Give the extent of all Trypanosoma brucei.
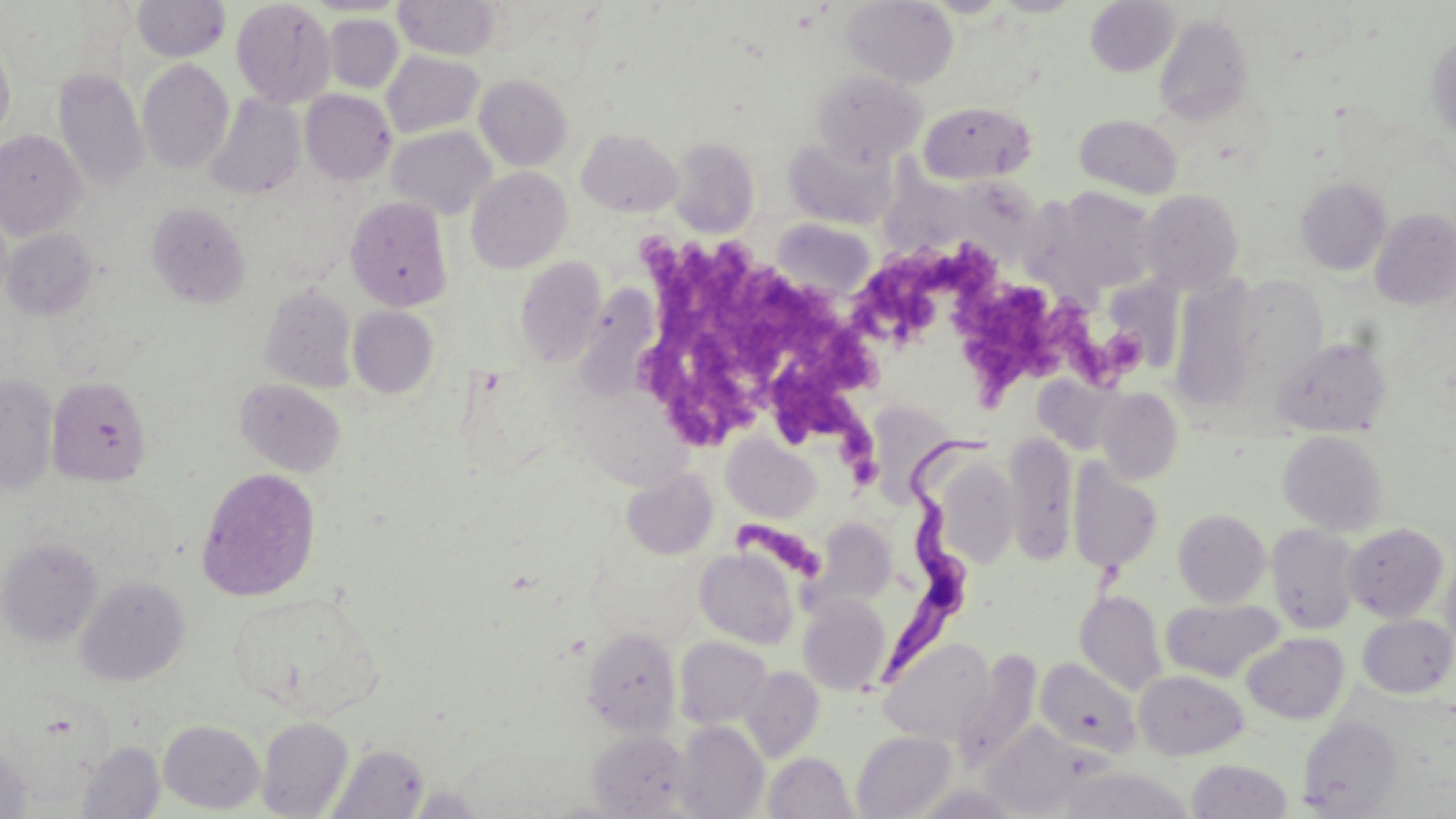
Approximate bounding boxes as [x1, y1, x2, y2] in pixels.
Trypanosoma brucei: [879, 432, 1000, 686].

Platelet locations: [631, 230, 779, 440], [865, 250, 996, 342], [772, 279, 886, 483], [960, 281, 1079, 404], [1059, 307, 1142, 388], [731, 523, 823, 577]. Uninfected red blood cell locations: [132, 0, 231, 62], [393, 0, 501, 60], [920, 0, 1015, 18], [991, 0, 1087, 16], [232, 1, 336, 108], [842, 1, 959, 88], [1085, 1, 1180, 77], [325, 14, 403, 94], [1154, 14, 1254, 125], [1426, 32, 1456, 141], [0, 40, 15, 145], [381, 51, 484, 138], [137, 59, 234, 174], [53, 69, 148, 191], [811, 69, 927, 167], [474, 75, 573, 171], [301, 89, 396, 185], [205, 94, 305, 199], [919, 101, 1037, 184], [1075, 114, 1183, 199], [387, 126, 496, 220], [577, 128, 682, 217], [0, 130, 88, 240], [669, 137, 760, 237], [784, 137, 898, 230], [882, 152, 971, 258], [466, 166, 572, 273], [963, 172, 1059, 274], [1296, 177, 1392, 276], [1049, 187, 1158, 291], [1140, 190, 1244, 294], [345, 196, 452, 311], [147, 201, 251, 309], [1370, 207, 1456, 311], [772, 218, 876, 302], [2, 228, 97, 321], [515, 256, 607, 367], [1228, 275, 1328, 385], [1103, 279, 1184, 372], [1172, 279, 1258, 412], [259, 282, 357, 393], [347, 306, 439, 398], [1272, 336, 1392, 438], [0, 373, 58, 495], [47, 376, 152, 487], [234, 379, 346, 477], [1097, 387, 1184, 484], [870, 401, 959, 505], [1278, 431, 1389, 535], [1004, 432, 1077, 564], [723, 436, 821, 523], [935, 457, 1019, 568], [1068, 460, 1162, 574], [196, 467, 321, 601], [621, 469, 717, 560], [1173, 509, 1271, 608], [810, 518, 896, 611], [1343, 523, 1449, 622], [1266, 524, 1362, 634], [1, 537, 103, 647], [694, 547, 799, 649], [1440, 553, 1456, 657], [76, 576, 190, 686], [227, 589, 383, 720], [1075, 590, 1167, 695], [797, 594, 891, 695], [1161, 598, 1284, 683], [1357, 614, 1456, 698], [582, 627, 681, 737], [1242, 632, 1349, 724], [674, 636, 772, 729], [880, 638, 995, 746], [953, 647, 1041, 770], [1036, 657, 1141, 757], [740, 666, 824, 762], [1134, 670, 1248, 760], [1298, 715, 1404, 817], [256, 717, 354, 818], [158, 720, 265, 813], [673, 721, 769, 818], [982, 727, 1088, 813], [588, 729, 691, 818], [851, 730, 957, 818], [0, 741, 31, 818], [76, 742, 165, 818], [326, 744, 429, 819], [763, 751, 858, 819], [1185, 759, 1294, 819], [407, 785, 484, 816]. Slide-level diagnosis: Trypanosoma brucei. 1000x magnification. Single field of view. May-Grünwald-Giemsa-stained preparation. Thin blood smear. Image is 1456×819 pixels. Light microscopy.